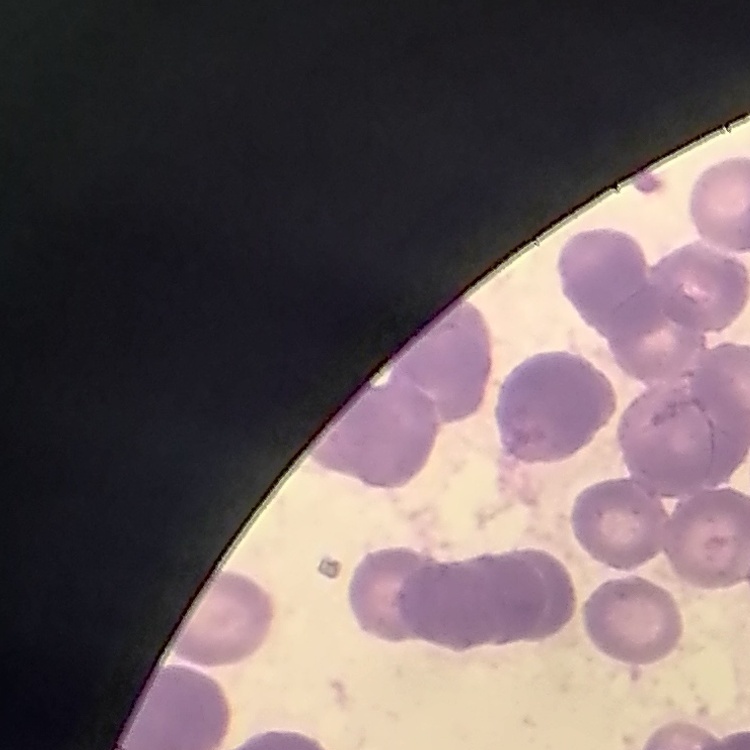

Summary:
  - Erythrocyte morphology: rouleaux formation
  - Image type: square crop of a larger photomicrograph
  - Stain: Field's or Giemsa
  - Preparation: thin blood film